Assess the morphology of the erythrocytes.
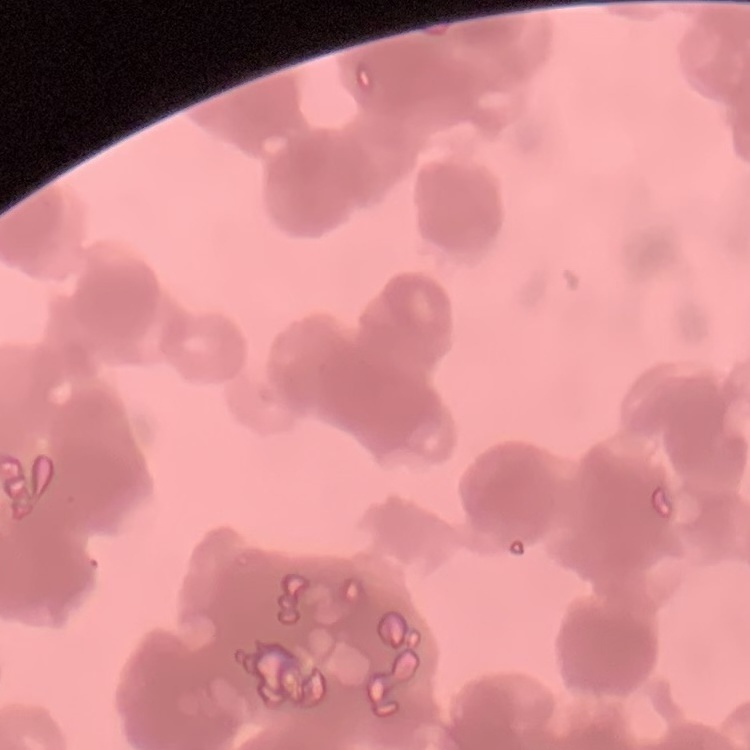

They show rouleaux formation.

Summary:
  - Preparation: thin blood film
  - Image type: one tile cut from a larger photomicrograph
  - Stain: Field's or Giemsa